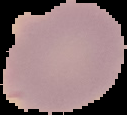

{
  "image_size": "127×115 pixels",
  "image_type": "cell region segmented out of the field of view; surrounding area masked to black",
  "preparation": "thin blood smear",
  "malaria_status": "uninfected"
}